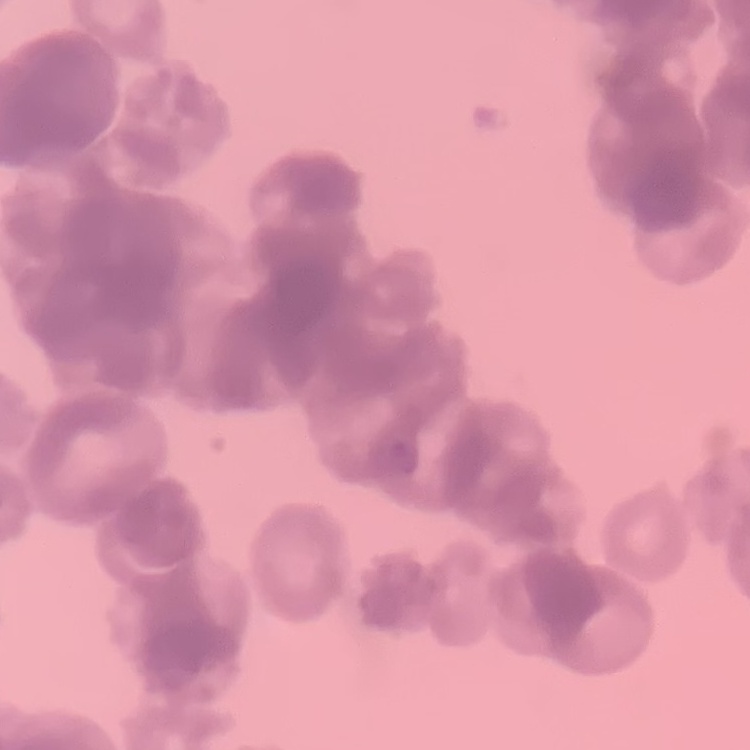

red blood cell morphology = rouleaux formation
image type = square crop of a larger photomicrograph
preparation = thin blood film
stain = Field's or Giemsa